Comment on the morphology of the red blood cells.
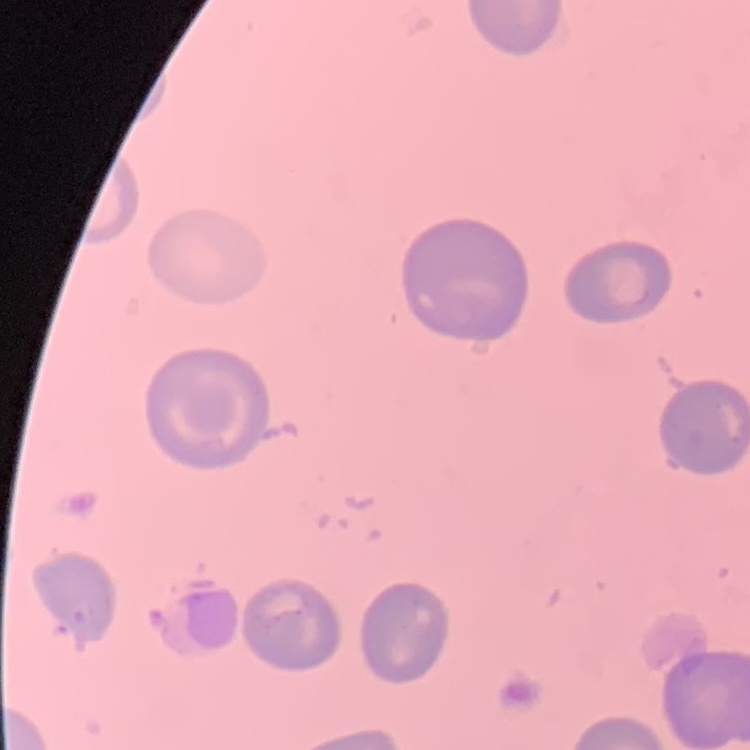

No rouleaux formation.

Summary:
  - Stain: Field's or Giemsa
  - Preparation: thin blood smear
  - Image type: one tile cut from a larger photomicrograph